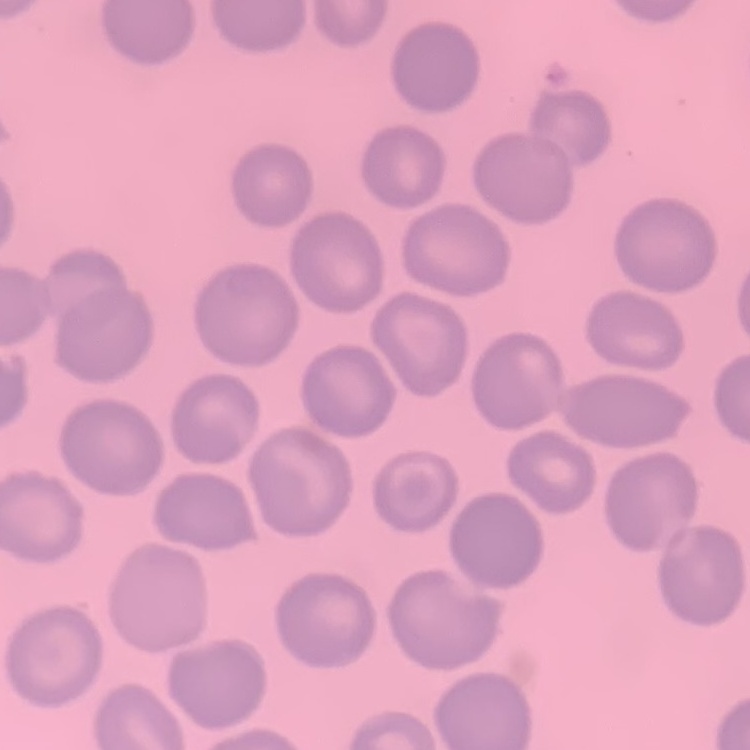

erythrocyte_morphology: no rouleaux formation
preparation: thin blood smear
image_type: one tile cut from a larger photomicrograph
stain: Field's or Giemsa